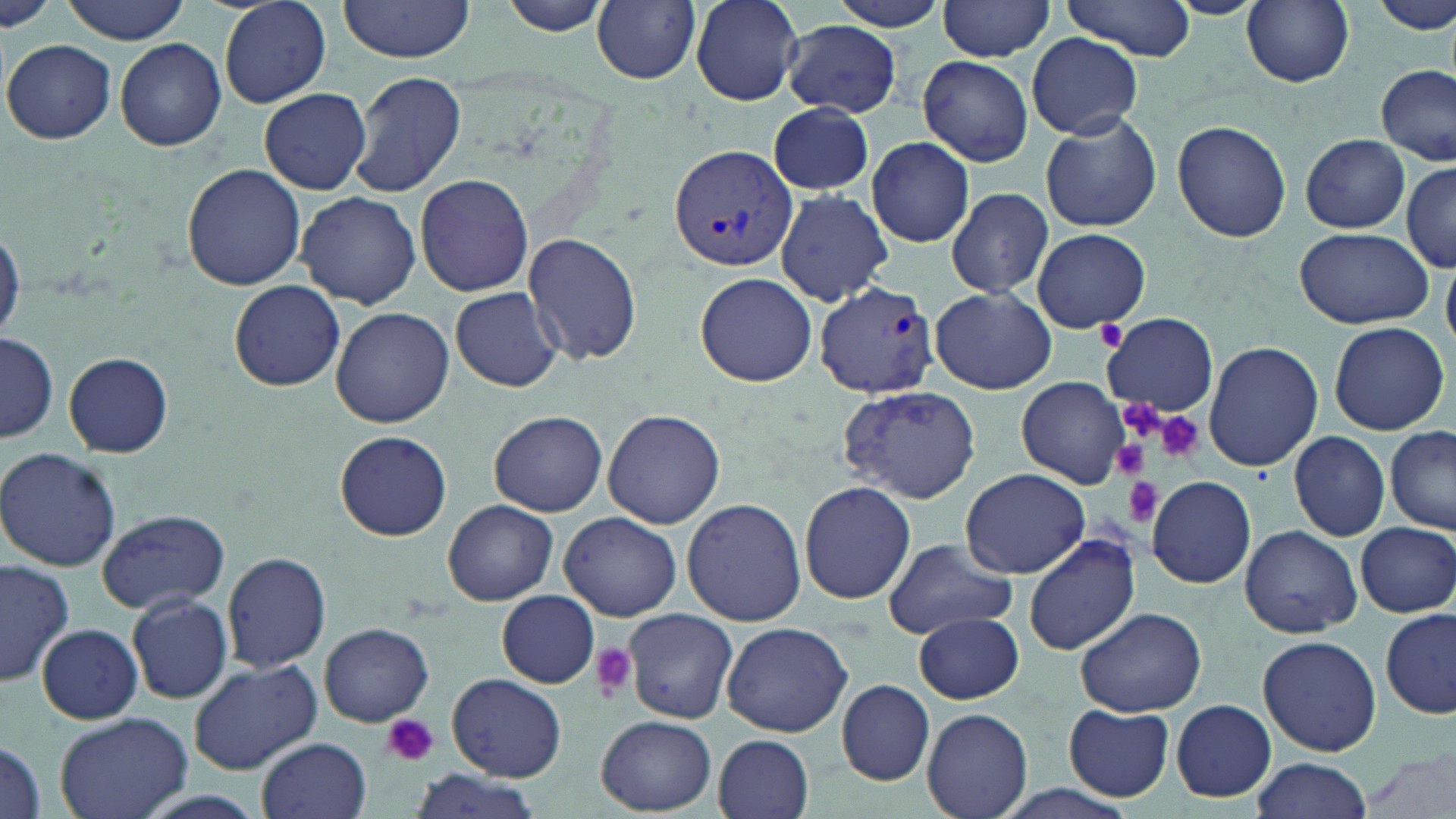
slide-level diagnosis = Plasmodium vivax
modality = optical microscopy
field of view = one of a larger specimen
platelet locations = approximate bounding boxes as named x1/y1/x2/y2 corners in pixels: (x1=1151, y1=409, x2=1206, y2=464), (x1=1109, y1=439, x2=1153, y2=481), (x1=1124, y1=479, x2=1163, y2=527), (x1=587, y1=643, x2=638, y2=699), (x1=383, y1=714, x2=440, y2=767)
Plasmodium vivax-infected red blood cell locations = approximate bounding boxes as named x1/y1/x2/y2 corners in pixels: (x1=670, y1=143, x2=800, y2=272), (x1=814, y1=280, x2=940, y2=398)
stain = May-Grünwald-Giemsa
magnification = 1000x
uninfected red blood cell locations = approximate bounding boxes as named x1/y1/x2/y2 corners in pixels: (x1=61, y1=0, x2=191, y2=43), (x1=218, y1=0, x2=333, y2=108), (x1=496, y1=0, x2=621, y2=36), (x1=691, y1=0, x2=805, y2=105), (x1=1373, y1=0, x2=1456, y2=36), (x1=336, y1=1, x2=478, y2=67), (x1=592, y1=1, x2=700, y2=84), (x1=826, y1=1, x2=955, y2=32), (x1=937, y1=1, x2=1056, y2=59), (x1=1059, y1=1, x2=1198, y2=61), (x1=1241, y1=1, x2=1356, y2=87), (x1=0, y1=3, x2=57, y2=34), (x1=783, y1=20, x2=901, y2=117), (x1=1026, y1=32, x2=1142, y2=138), (x1=115, y1=37, x2=226, y2=151), (x1=4, y1=39, x2=117, y2=143), (x1=918, y1=55, x2=1034, y2=166), (x1=1377, y1=63, x2=1454, y2=166), (x1=347, y1=69, x2=469, y2=198), (x1=259, y1=87, x2=371, y2=195), (x1=768, y1=101, x2=875, y2=195), (x1=1040, y1=109, x2=1162, y2=232), (x1=1172, y1=119, x2=1291, y2=243), (x1=1301, y1=134, x2=1410, y2=235), (x1=865, y1=136, x2=975, y2=247), (x1=1399, y1=163, x2=1456, y2=271), (x1=182, y1=164, x2=304, y2=290), (x1=414, y1=173, x2=535, y2=296), (x1=946, y1=187, x2=1054, y2=299), (x1=775, y1=188, x2=893, y2=307), (x1=297, y1=190, x2=421, y2=311), (x1=0, y1=224, x2=23, y2=344), (x1=1294, y1=226, x2=1433, y2=329), (x1=1031, y1=227, x2=1151, y2=333), (x1=522, y1=233, x2=644, y2=367), (x1=696, y1=273, x2=816, y2=385), (x1=229, y1=280, x2=344, y2=391), (x1=449, y1=287, x2=565, y2=392), (x1=930, y1=287, x2=1057, y2=394), (x1=330, y1=306, x2=453, y2=428), (x1=1102, y1=313, x2=1218, y2=416), (x1=1329, y1=322, x2=1452, y2=435), (x1=1, y1=331, x2=57, y2=443), (x1=1202, y1=341, x2=1323, y2=471), (x1=64, y1=352, x2=174, y2=457), (x1=1016, y1=376, x2=1132, y2=489), (x1=837, y1=384, x2=981, y2=503), (x1=602, y1=409, x2=726, y2=529), (x1=489, y1=410, x2=607, y2=517), (x1=1386, y1=425, x2=1456, y2=533), (x1=335, y1=430, x2=451, y2=541), (x1=1289, y1=432, x2=1390, y2=540), (x1=0, y1=446, x2=121, y2=574), (x1=960, y1=468, x2=1092, y2=579), (x1=1147, y1=474, x2=1257, y2=588), (x1=799, y1=481, x2=916, y2=605), (x1=681, y1=498, x2=806, y2=624), (x1=443, y1=499, x2=559, y2=605), (x1=97, y1=508, x2=229, y2=614), (x1=560, y1=510, x2=682, y2=621), (x1=1355, y1=521, x2=1456, y2=618), (x1=1239, y1=523, x2=1361, y2=638), (x1=1023, y1=532, x2=1141, y2=657), (x1=881, y1=536, x2=1018, y2=639), (x1=222, y1=550, x2=331, y2=674), (x1=0, y1=557, x2=76, y2=686), (x1=498, y1=591, x2=601, y2=687), (x1=127, y1=594, x2=232, y2=703), (x1=1073, y1=607, x2=1207, y2=717), (x1=623, y1=609, x2=736, y2=723), (x1=1380, y1=609, x2=1456, y2=722), (x1=915, y1=613, x2=1025, y2=705), (x1=37, y1=623, x2=143, y2=722), (x1=319, y1=623, x2=432, y2=724), (x1=719, y1=624, x2=852, y2=736), (x1=1259, y1=634, x2=1382, y2=756), (x1=186, y1=658, x2=323, y2=774), (x1=447, y1=673, x2=566, y2=782), (x1=836, y1=679, x2=935, y2=784), (x1=1170, y1=699, x2=1277, y2=802), (x1=1063, y1=703, x2=1176, y2=801), (x1=923, y1=708, x2=1032, y2=819), (x1=54, y1=710, x2=192, y2=819), (x1=597, y1=714, x2=714, y2=815), (x1=715, y1=734, x2=815, y2=819), (x1=259, y1=736, x2=372, y2=819), (x1=0, y1=737, x2=47, y2=819), (x1=1364, y1=750, x2=1455, y2=819), (x1=1249, y1=758, x2=1374, y2=819), (x1=404, y1=767, x2=550, y2=819)
image size = 1456×819 pixels
preparation = thin blood film